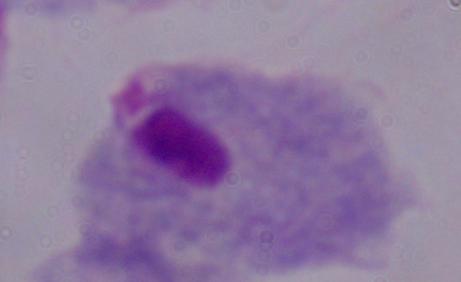

Summary:
  - Modality: micrograph
  - Identification: trichomonad
  - Magnification: 1000x